Comment on the morphology of the red blood cells.
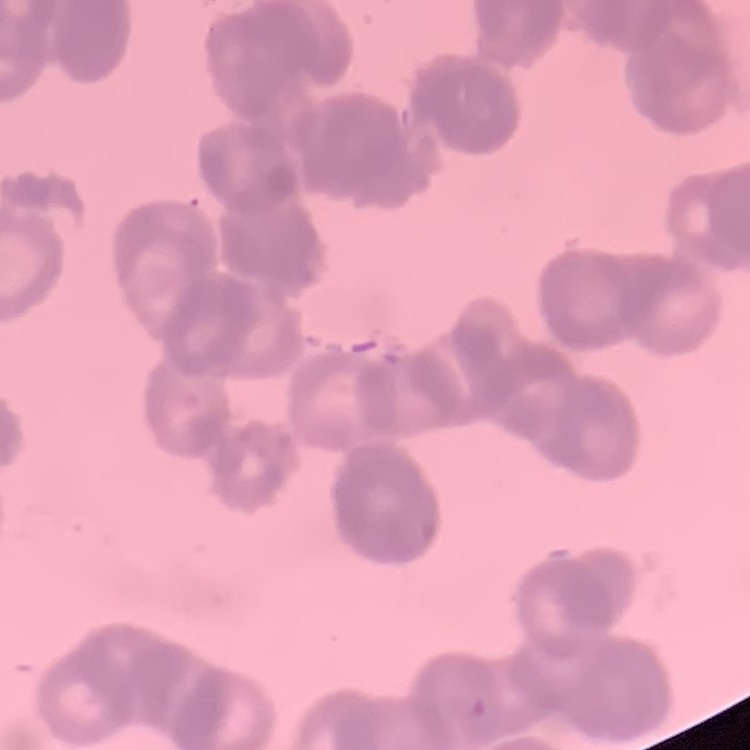

Rouleaux formation.

Summary:
  - Preparation: thin blood smear
  - Image type: square crop of a larger photomicrograph
  - Stain: Field's or Giemsa